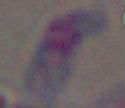
Captured at 1000x magnification. Photomicrograph. Toxoplasma gondii is seen.